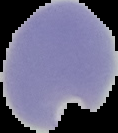
Malaria status: parasitized. The area outside the segmented cell region is set to black. From a thin blood smear. Image is 118×133 pixels.